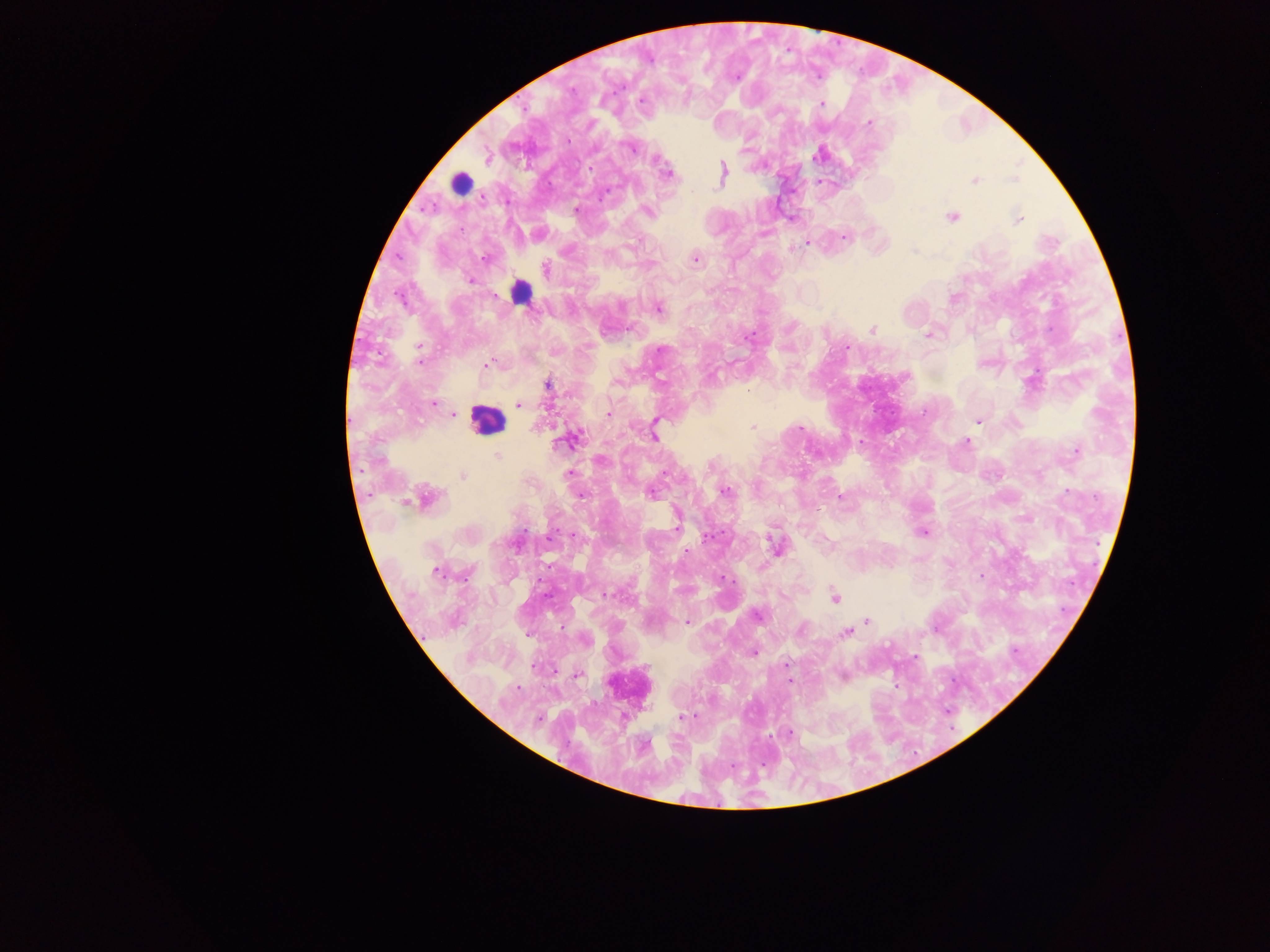

{
  "preparation": "thick blood film",
  "capture": "mobile-phone photograph through a microscope",
  "plasmodium_parasite_locations": "approximate centers as x y in pixels: 641 100; 821 105; 869 123; 567 138; 631 146; 820 154; 487 155; 668 174; 722 174; 974 180; 577 209; 647 212; 951 216; 791 217; 1018 218; 764 232; 538 234; 846 236; 806 242; 695 258; 544 269; 470 280; 658 308; 872 330; 929 334; 846 347; 488 364; 547 382; 433 403; 519 404; 454 413; 608 414; 978 421; 753 427; 653 435; 570 440; 966 443; 1076 450; 497 456; 567 474; 462 476; 724 490; 651 492; 581 494; 839 497; 420 498; 676 523; 923 531; 573 534; 776 547; 686 551; 437 572; 980 576; 721 577; 604 594; 834 597; 756 614; 687 621; 867 621; 845 632; 584 640; 753 651; 916 657; 786 664; 577 674; 842 676; 789 680; 680 718; 789 734",
  "image_size": "1270×952 pixels",
  "field_of_view": "single",
  "country": "Ghana",
  "leukocyte_locations": "approximate centers as x y in pixels: 460 183; 521 291; 487 420; 628 687"
}